Classify this cell by malaria status.
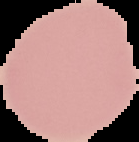

Uninfected.

Summary:
  - Image type: segmented cell region with the area outside set to black
  - Image size: 139×142 pixels
  - Preparation: thin blood smear